Report the malaria status of this cell.
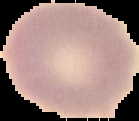
Uninfected.

From a thin blood smear. The area outside the segmented cell region is set to black. Image is 139×121 pixels.